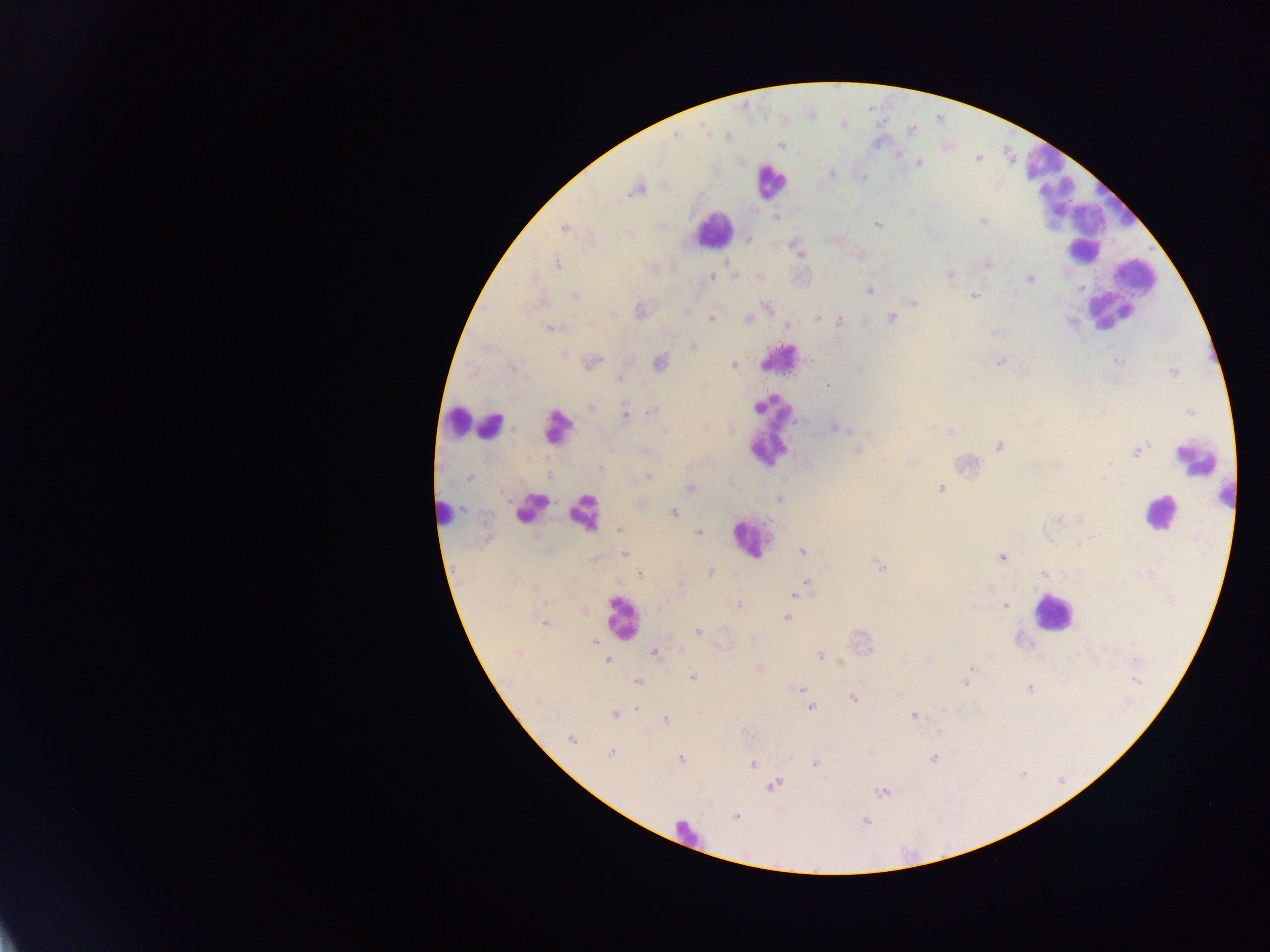
Approximate centers as (x, y) in pixels. Leukocyte locations (subset; some below the resolvable size): (769, 181), (1046, 187), (1116, 202), (713, 229), (1083, 251), (1113, 293), (780, 360), (457, 420), (492, 427), (560, 427), (775, 430), (1195, 458), (1226, 498), (533, 507), (582, 510), (442, 512), (1158, 513), (749, 539), (1051, 611), (620, 617), (687, 833). Plasmodium parasite locations: (676, 135), (727, 138), (780, 145), (919, 163), (832, 173), (863, 176), (637, 189), (776, 216), (983, 220), (877, 224), (564, 228), (748, 239), (799, 252), (727, 262), (556, 263), (988, 263), (734, 275), (950, 275), (712, 276), (760, 276), (1030, 278), (869, 290), (574, 295), (974, 296), (913, 302), (766, 306), (686, 310), (640, 311), (817, 317), (892, 317), (711, 318), (748, 319), (839, 320), (786, 325), (550, 328), (693, 347), (592, 362), (999, 362), (660, 363), (733, 365), (513, 367), (620, 378), (827, 385), (590, 406), (652, 411), (1191, 412), (625, 415), (835, 427), (930, 427), (950, 431), (665, 432), (1000, 446), (858, 449), (643, 451), (1138, 452), (885, 460), (1056, 466), (601, 468), (550, 476), (649, 476), (470, 477), (1105, 478), (691, 488), (941, 489), (780, 498), (674, 512), (620, 529), (699, 533), (802, 552), (623, 555), (1002, 557), (880, 565), (710, 573), (639, 574), (1044, 574), (806, 581), (681, 585), (795, 595), (1004, 605), (738, 606), (787, 618), (542, 622), (698, 632), (594, 640), (655, 652), (820, 656), (929, 660), (608, 661), (759, 668), (971, 668), (693, 677), (637, 681), (1136, 681), (965, 682), (1029, 687), (802, 689), (536, 700), (855, 700), (810, 707), (637, 708), (614, 714), (914, 715), (665, 720), (572, 739), (611, 754), (933, 759), (681, 760), (752, 763), (815, 763), (775, 785), (883, 792), (735, 816), (866, 821). Photographed through a microscope with a mobile-phone camera. Image is 1270×952 pixels. Thick blood film. One field of view. Collected in Ghana.